Locate every Plasmodium parasite.
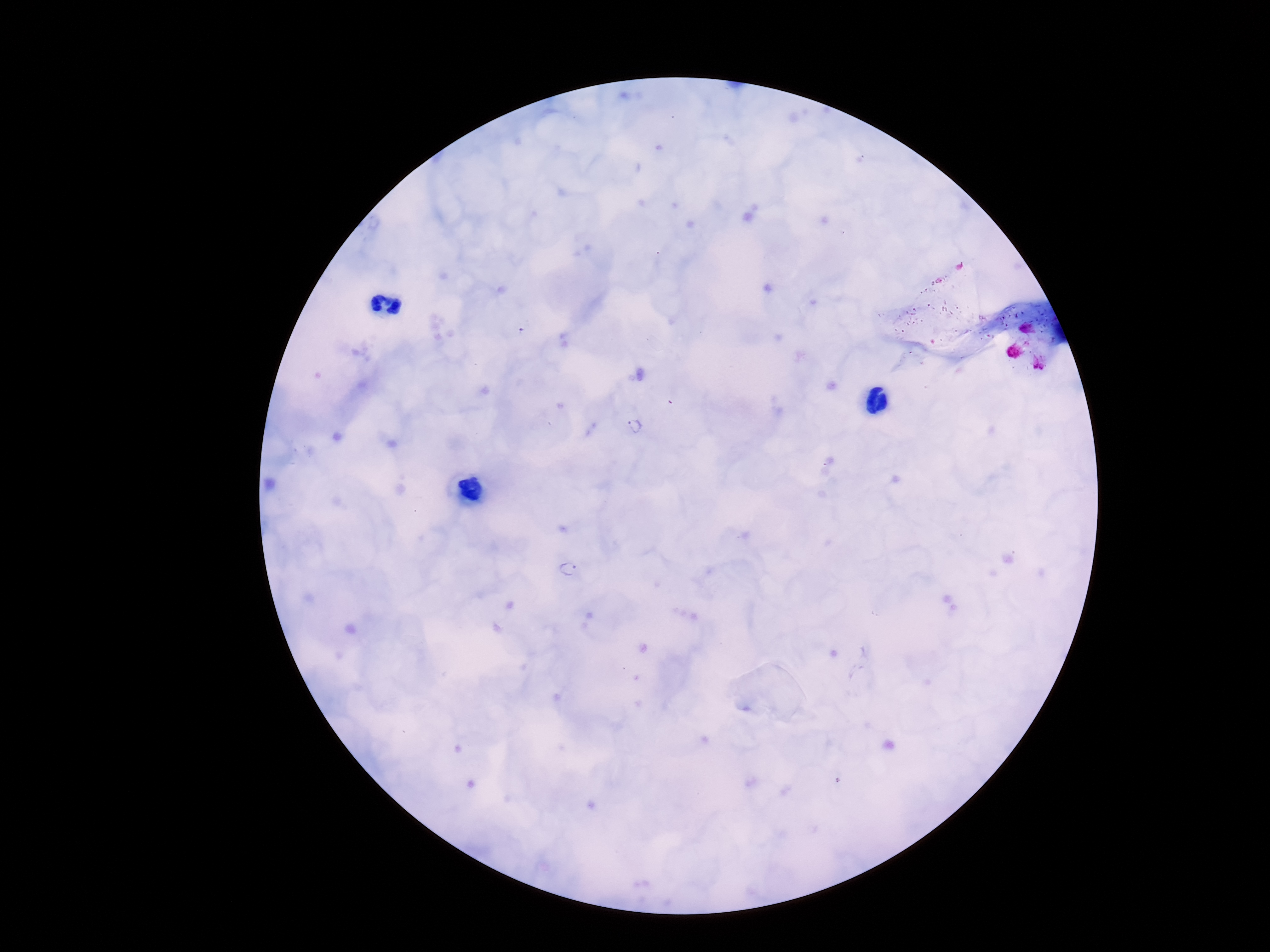

Approximate centers as {x, y} in pixels.
Plasmodium parasites: {637, 426}, {567, 569}.

One field from this slide. Giemsa stain. Thick blood smear. Image is 1270×952 pixels. Patient malaria status: infected. Smartphone photograph taken through the microscope eyepiece. 100x magnification.